Locate platelets.
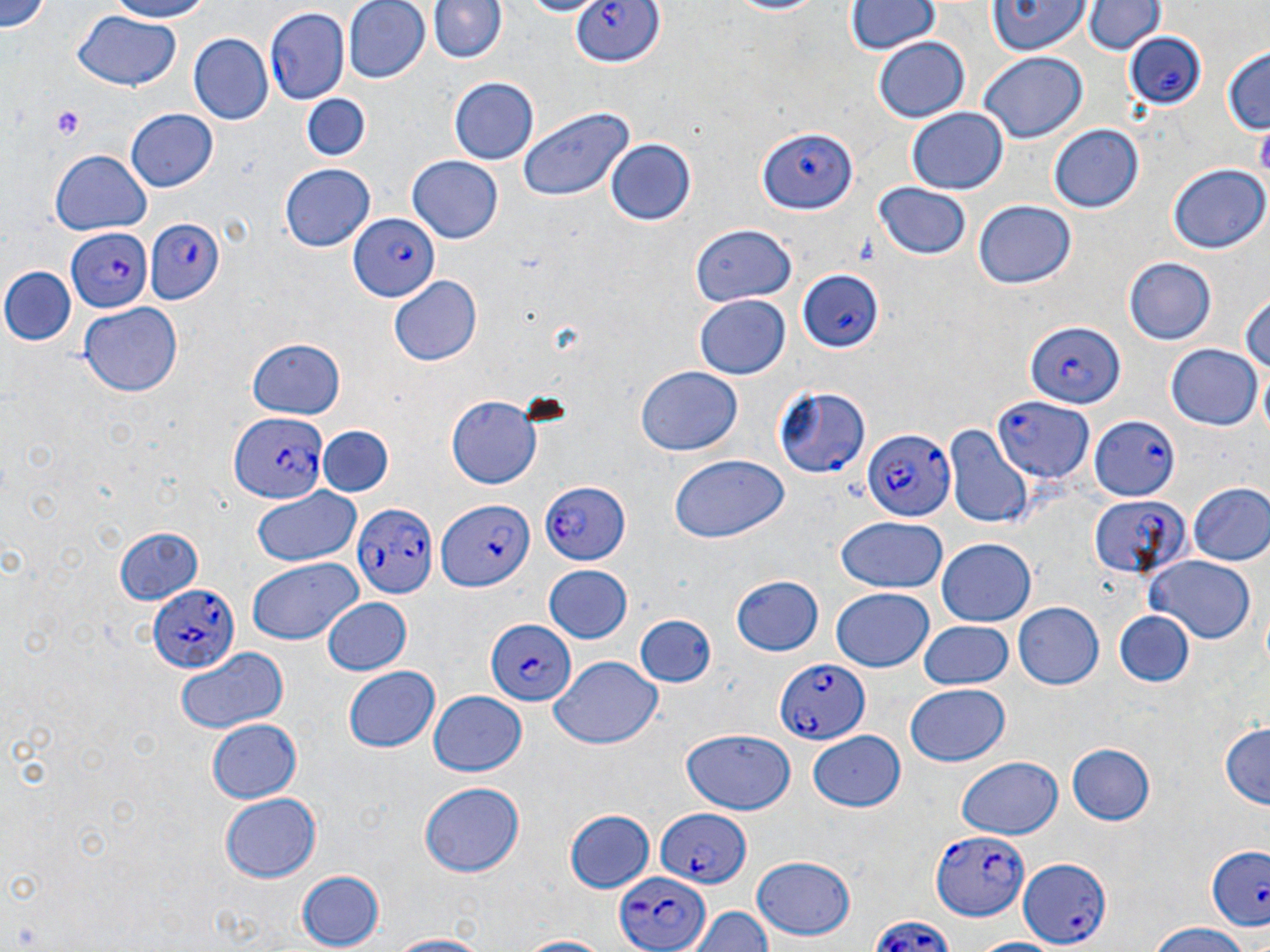

Approximate bounding boxes as named x1/y1/x2/y2 corners in pixels.
Platelets: (x1=51, y1=108, x2=84, y2=138).

Summary:
  - Uninfected red blood cell locations (subset): (x1=3, y1=0, x2=53, y2=35), (x1=98, y1=0, x2=215, y2=23), (x1=342, y1=0, x2=433, y2=85), (x1=429, y1=0, x2=506, y2=65), (x1=716, y1=0, x2=830, y2=17), (x1=988, y1=0, x2=1090, y2=55), (x1=514, y1=1, x2=603, y2=18), (x1=1085, y1=1, x2=1163, y2=56), (x1=844, y1=2, x2=938, y2=56), (x1=72, y1=11, x2=183, y2=90), (x1=187, y1=32, x2=272, y2=123), (x1=872, y1=37, x2=971, y2=122), (x1=1220, y1=48, x2=1270, y2=138), (x1=979, y1=53, x2=1088, y2=144), (x1=451, y1=77, x2=539, y2=166), (x1=302, y1=94, x2=371, y2=163), (x1=519, y1=104, x2=637, y2=204), (x1=906, y1=108, x2=1008, y2=194), (x1=126, y1=109, x2=219, y2=192), (x1=1050, y1=124, x2=1146, y2=213), (x1=607, y1=139, x2=695, y2=226), (x1=49, y1=149, x2=153, y2=235), (x1=406, y1=156, x2=501, y2=244), (x1=280, y1=162, x2=374, y2=251), (x1=1166, y1=162, x2=1268, y2=255), (x1=873, y1=183, x2=974, y2=264), (x1=972, y1=200, x2=1075, y2=288), (x1=692, y1=226, x2=797, y2=306), (x1=1122, y1=254, x2=1217, y2=343), (x1=3, y1=266, x2=75, y2=346), (x1=389, y1=277, x2=483, y2=366), (x1=1239, y1=290, x2=1270, y2=380), (x1=694, y1=296, x2=790, y2=381), (x1=79, y1=302, x2=184, y2=395), (x1=248, y1=333, x2=346, y2=418), (x1=1165, y1=345, x2=1262, y2=429), (x1=636, y1=367, x2=744, y2=456), (x1=446, y1=397, x2=547, y2=489), (x1=944, y1=425, x2=1032, y2=527), (x1=317, y1=426, x2=394, y2=498), (x1=668, y1=454, x2=788, y2=542), (x1=1188, y1=483, x2=1270, y2=567), (x1=251, y1=486, x2=362, y2=568), (x1=834, y1=519, x2=948, y2=596), (x1=114, y1=525, x2=207, y2=605), (x1=937, y1=538, x2=1036, y2=628), (x1=1143, y1=554, x2=1259, y2=642), (x1=247, y1=559, x2=362, y2=645), (x1=544, y1=565, x2=633, y2=645), (x1=732, y1=576, x2=823, y2=658), (x1=830, y1=587, x2=934, y2=672), (x1=322, y1=599, x2=412, y2=676), (x1=1012, y1=603, x2=1103, y2=690), (x1=1112, y1=610, x2=1195, y2=690), (x1=633, y1=615, x2=717, y2=689), (x1=919, y1=620, x2=1014, y2=690), (x1=173, y1=645, x2=286, y2=735), (x1=550, y1=655, x2=663, y2=750), (x1=341, y1=666, x2=438, y2=754), (x1=904, y1=684, x2=1011, y2=768), (x1=428, y1=691, x2=528, y2=777), (x1=204, y1=718, x2=303, y2=804), (x1=1220, y1=721, x2=1270, y2=809), (x1=679, y1=728, x2=796, y2=816), (x1=804, y1=730, x2=908, y2=812), (x1=1066, y1=740, x2=1155, y2=825), (x1=957, y1=757, x2=1063, y2=840), (x1=420, y1=781, x2=527, y2=878), (x1=220, y1=794, x2=321, y2=881), (x1=564, y1=808, x2=655, y2=894), (x1=750, y1=856, x2=853, y2=941), (x1=297, y1=869, x2=386, y2=949), (x1=686, y1=904, x2=774, y2=952), (x1=1144, y1=924, x2=1252, y2=952), (x1=381, y1=933, x2=496, y2=952), (x1=511, y1=934, x2=620, y2=952), (x1=965, y1=937, x2=1063, y2=952)
  - Plasmodium falciparum-infected red blood cell locations (subset): (x1=571, y1=0, x2=663, y2=69), (x1=264, y1=5, x2=351, y2=105), (x1=1123, y1=31, x2=1209, y2=111), (x1=755, y1=128, x2=857, y2=216), (x1=351, y1=211, x2=440, y2=301), (x1=142, y1=217, x2=225, y2=306), (x1=65, y1=228, x2=149, y2=313), (x1=795, y1=267, x2=884, y2=351), (x1=1025, y1=320, x2=1124, y2=407), (x1=772, y1=386, x2=870, y2=479), (x1=995, y1=396, x2=1093, y2=482), (x1=1089, y1=408, x2=1189, y2=502), (x1=229, y1=413, x2=326, y2=506), (x1=862, y1=431, x2=958, y2=521), (x1=537, y1=481, x2=627, y2=564), (x1=1089, y1=492, x2=1188, y2=580), (x1=435, y1=499, x2=533, y2=594), (x1=351, y1=501, x2=435, y2=599), (x1=149, y1=584, x2=240, y2=675), (x1=485, y1=620, x2=576, y2=706), (x1=774, y1=658, x2=867, y2=746), (x1=656, y1=808, x2=751, y2=887), (x1=930, y1=829, x2=1026, y2=918), (x1=1207, y1=848, x2=1270, y2=928), (x1=1018, y1=857, x2=1111, y2=948), (x1=613, y1=870, x2=710, y2=952)
  - Slide-level diagnosis: Plasmodium falciparum
  - Preparation: thin blood smear
  - Stain: May-Grünwald-Giemsa
  - Modality: optical microscopy
  - Image size: 1270×952 pixels
  - Magnification: 1000x
  - Field of view: one of a larger specimen